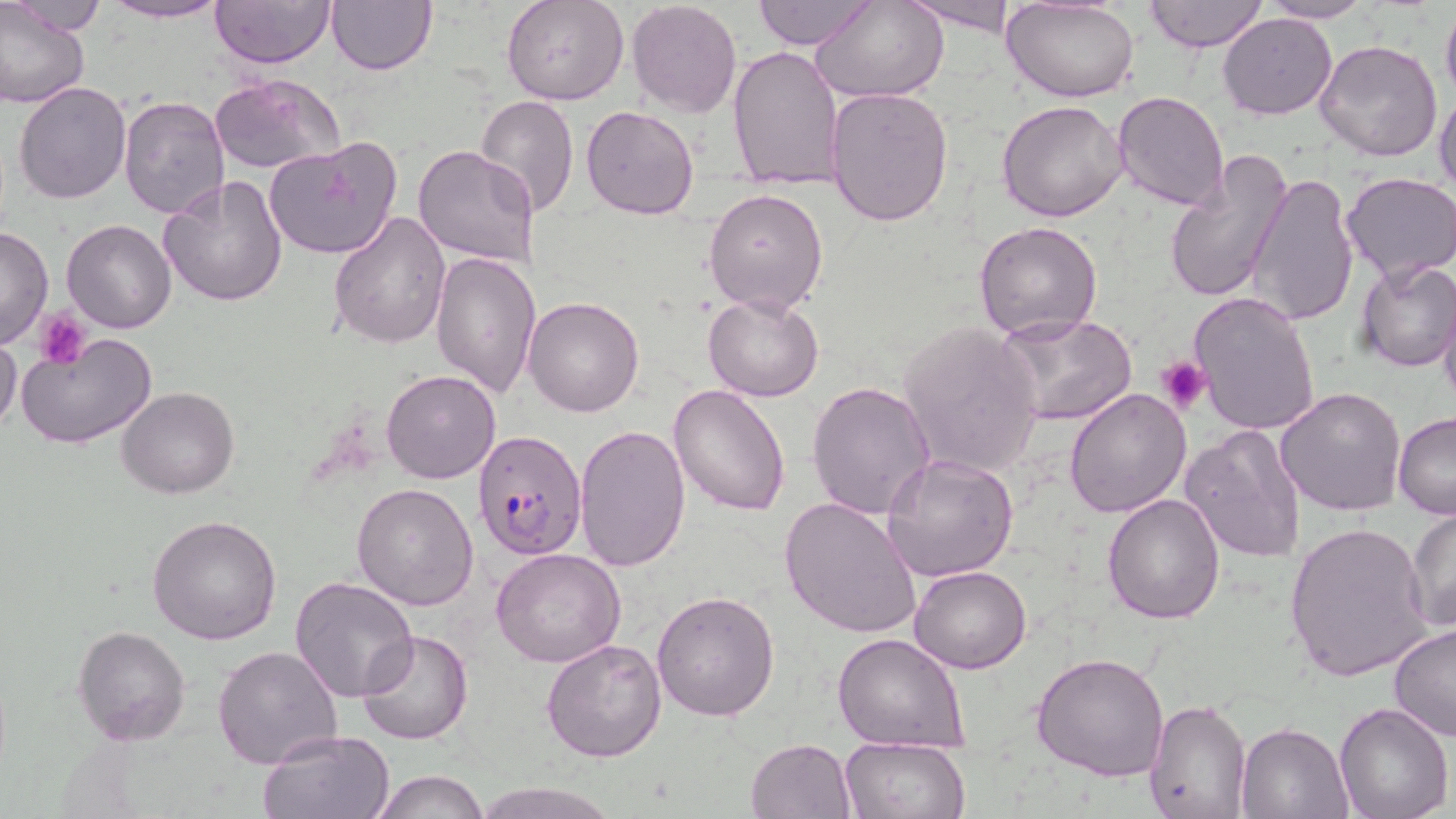
Approximate bounding boxes as named x1/y1/x2/y2 corners in pixels. Platelet locations: (x1=34, y1=310, x2=89, y2=367), (x1=1157, y1=356, x2=1212, y2=417). Uninfected red blood cell locations: (x1=7, y1=0, x2=106, y2=37), (x1=211, y1=0, x2=334, y2=68), (x1=325, y1=0, x2=438, y2=75), (x1=502, y1=0, x2=630, y2=106), (x1=627, y1=0, x2=742, y2=118), (x1=752, y1=0, x2=873, y2=50), (x1=814, y1=0, x2=948, y2=101), (x1=902, y1=0, x2=1019, y2=35), (x1=1147, y1=0, x2=1266, y2=52), (x1=102, y1=1, x2=230, y2=24), (x1=1258, y1=1, x2=1377, y2=24), (x1=1004, y1=2, x2=1139, y2=103), (x1=1441, y1=2, x2=1456, y2=107), (x1=0, y1=3, x2=89, y2=108), (x1=1217, y1=13, x2=1337, y2=120), (x1=1314, y1=40, x2=1443, y2=162), (x1=727, y1=44, x2=844, y2=190), (x1=210, y1=73, x2=343, y2=176), (x1=13, y1=81, x2=130, y2=204), (x1=1435, y1=83, x2=1456, y2=199), (x1=826, y1=87, x2=953, y2=226), (x1=1113, y1=90, x2=1231, y2=211), (x1=475, y1=95, x2=579, y2=215), (x1=118, y1=96, x2=231, y2=220), (x1=997, y1=101, x2=1129, y2=222), (x1=581, y1=105, x2=701, y2=219), (x1=264, y1=137, x2=403, y2=260), (x1=413, y1=145, x2=541, y2=270), (x1=1162, y1=152, x2=1293, y2=305), (x1=1245, y1=174, x2=1360, y2=327), (x1=1341, y1=174, x2=1456, y2=281), (x1=158, y1=175, x2=288, y2=306), (x1=703, y1=186, x2=830, y2=315), (x1=328, y1=210, x2=451, y2=348), (x1=62, y1=219, x2=178, y2=334), (x1=973, y1=220, x2=1103, y2=342), (x1=0, y1=225, x2=53, y2=348), (x1=429, y1=250, x2=540, y2=399), (x1=1354, y1=259, x2=1455, y2=373), (x1=1188, y1=290, x2=1321, y2=436), (x1=1439, y1=290, x2=1456, y2=414), (x1=702, y1=293, x2=825, y2=402), (x1=522, y1=296, x2=645, y2=417), (x1=993, y1=312, x2=1138, y2=427), (x1=897, y1=323, x2=1043, y2=479), (x1=12, y1=332, x2=158, y2=449), (x1=0, y1=334, x2=22, y2=437), (x1=382, y1=370, x2=501, y2=484), (x1=806, y1=381, x2=936, y2=521), (x1=668, y1=384, x2=791, y2=516), (x1=117, y1=387, x2=239, y2=497), (x1=1063, y1=387, x2=1191, y2=519), (x1=1275, y1=387, x2=1406, y2=517), (x1=1392, y1=412, x2=1456, y2=520), (x1=573, y1=424, x2=691, y2=571), (x1=1181, y1=424, x2=1307, y2=564), (x1=882, y1=452, x2=1019, y2=583), (x1=353, y1=482, x2=478, y2=610), (x1=1102, y1=492, x2=1225, y2=624), (x1=779, y1=496, x2=923, y2=638), (x1=1406, y1=505, x2=1455, y2=635), (x1=148, y1=514, x2=282, y2=646), (x1=1283, y1=520, x2=1433, y2=682), (x1=491, y1=546, x2=625, y2=667), (x1=909, y1=565, x2=1032, y2=674), (x1=290, y1=576, x2=420, y2=702), (x1=652, y1=590, x2=780, y2=721), (x1=73, y1=625, x2=190, y2=745), (x1=1388, y1=625, x2=1456, y2=742), (x1=358, y1=630, x2=472, y2=745), (x1=832, y1=634, x2=971, y2=750), (x1=541, y1=637, x2=667, y2=762), (x1=214, y1=644, x2=343, y2=769), (x1=1032, y1=649, x2=1171, y2=781), (x1=1144, y1=699, x2=1252, y2=818), (x1=1334, y1=702, x2=1453, y2=819), (x1=1238, y1=723, x2=1354, y2=817), (x1=260, y1=731, x2=393, y2=819), (x1=745, y1=737, x2=854, y2=819), (x1=839, y1=738, x2=969, y2=819), (x1=372, y1=770, x2=491, y2=818), (x1=473, y1=780, x2=616, y2=819). Plasmodium falciparum-infected red blood cell locations: (x1=471, y1=429, x2=587, y2=559). Slide-level diagnosis: Plasmodium falciparum. Image is 1456×819 pixels. Single field of view. Thin blood film. Captured at 1000x magnification. Optical microscopy. May-Grünwald-Giemsa stain.